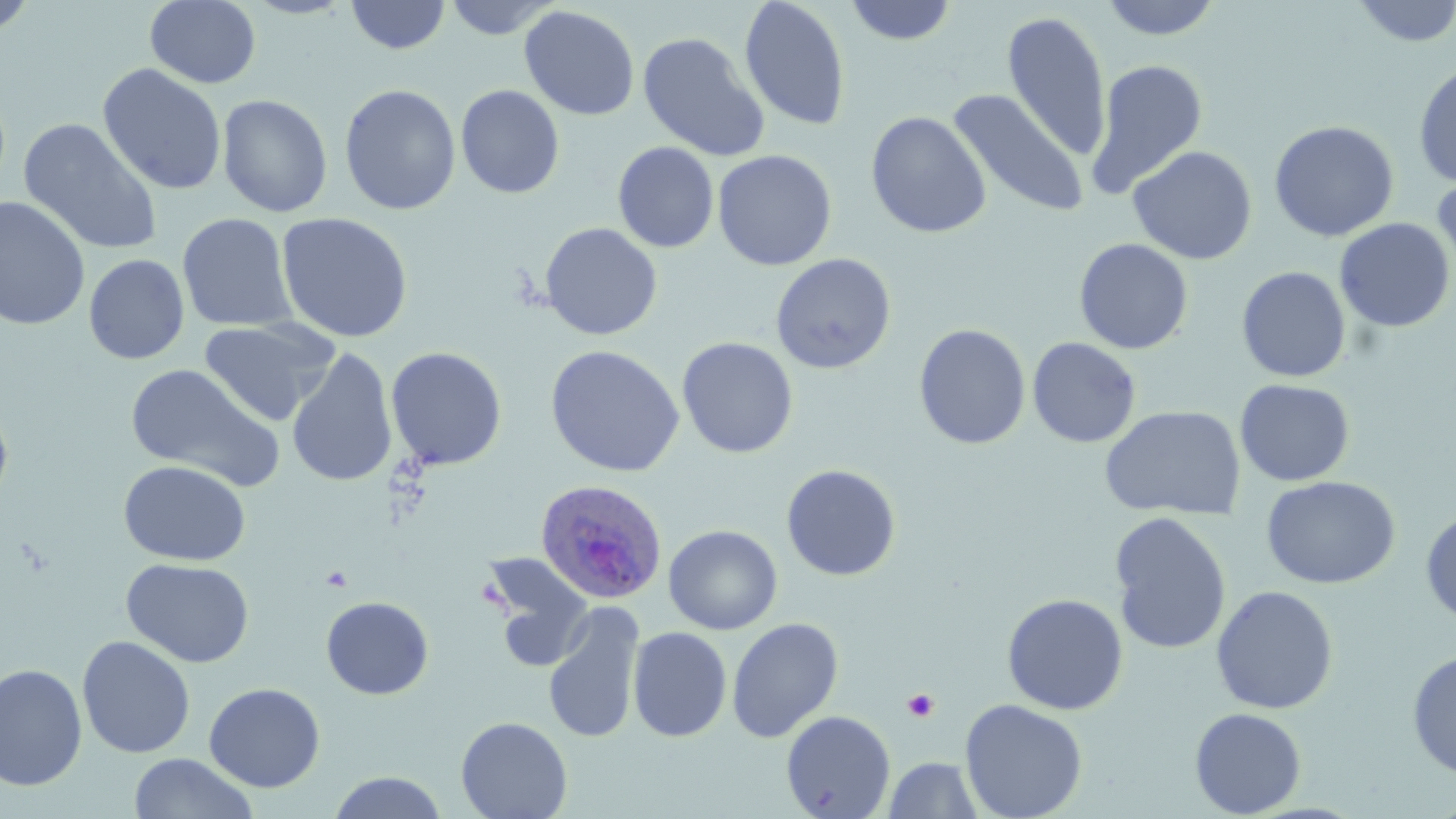
Summary:
  - Coordinate format: approximate bounding boxes as (x1,y1)-(x2,y2) corner pairs in pixels
  - Uninfected red blood cell locations: (0,0)-(39,36), (145,0)-(261,88), (442,0)-(561,40), (739,0)-(851,131), (1098,0)-(1224,41), (1351,0)-(1456,47), (345,1)-(451,55), (843,1)-(959,46), (518,5)-(640,120), (1001,11)-(1112,161), (637,31)-(770,161), (1087,58)-(1209,198), (1413,61)-(1456,189), (98,63)-(227,196), (339,83)-(461,215), (455,84)-(564,198), (947,88)-(1089,217), (217,94)-(333,218), (865,111)-(992,239), (18,118)-(163,256), (1268,120)-(1399,242), (612,141)-(719,252), (1127,145)-(1257,265), (713,149)-(837,271), (1431,168)-(1456,283), (0,196)-(91,331), (276,212)-(413,343), (177,213)-(298,332), (1335,218)-(1454,333), (539,222)-(663,341), (1073,238)-(1194,354), (770,253)-(897,374), (83,254)-(189,364), (1236,266)-(1351,382), (198,318)-(340,426), (913,323)-(1031,450), (677,337)-(798,458), (1027,337)-(1141,448), (545,344)-(685,478), (386,347)-(507,470), (286,348)-(397,488), (125,363)-(284,491), (1235,379)-(1355,486), (0,398)-(14,510), (1099,405)-(1247,521), (118,460)-(251,566), (781,464)-(901,581), (1261,476)-(1400,589), (1420,508)-(1455,629), (1108,511)-(1232,655), (663,525)-(783,635), (478,551)-(597,672), (121,557)-(255,668), (1210,585)-(1339,714), (1001,593)-(1128,715), (321,596)-(434,699), (542,604)-(645,742), (726,617)-(844,743), (627,627)-(732,742), (77,635)-(196,758), (1407,650)-(1456,779), (0,662)-(87,791), (204,682)-(325,792), (959,698)-(1088,818), (1189,708)-(1307,817), (781,710)-(896,818), (455,716)-(573,819), (127,752)-(259,819), (882,757)-(985,818), (326,771)-(450,818)
  - Plasmodium ovale-infected red blood cell locations: (533,478)-(666,605)
  - Platelet locations: (902,688)-(940,722)
  - Slide-level diagnosis: Plasmodium ovale
  - Stain: May-Grünwald-Giemsa
  - Magnification: 1000x
  - Field of view: one of a larger specimen
  - Image size: 1456×819 pixels
  - Modality: light microscopy
  - Preparation: thin blood smear